Assess this cell for malaria.
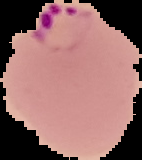

It is parasitized.

{
  "preparation": "thin blood smear",
  "image_type": "segmented cell region with the area outside set to black",
  "image_size": "142×160 pixels"
}